Locate Plasmodium parasites and leukocytes.
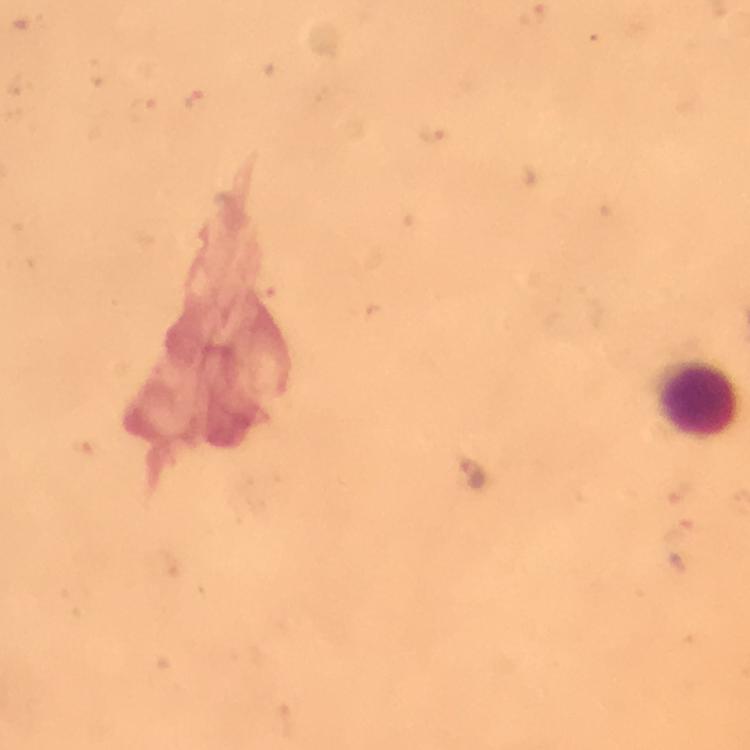

Approximate centers as {x, y} in pixels.
Plasmodium parasites: {473, 474}.
Leukocytes: {698, 398}.

cropped_from: one field of view
context: from a malaria diagnostic workup
stain: Giemsa
immersion_oil: applied
preparation: thick smear
magnification: 100x
capture: smartphone camera through the microscope
image_size: 750×750 pixels